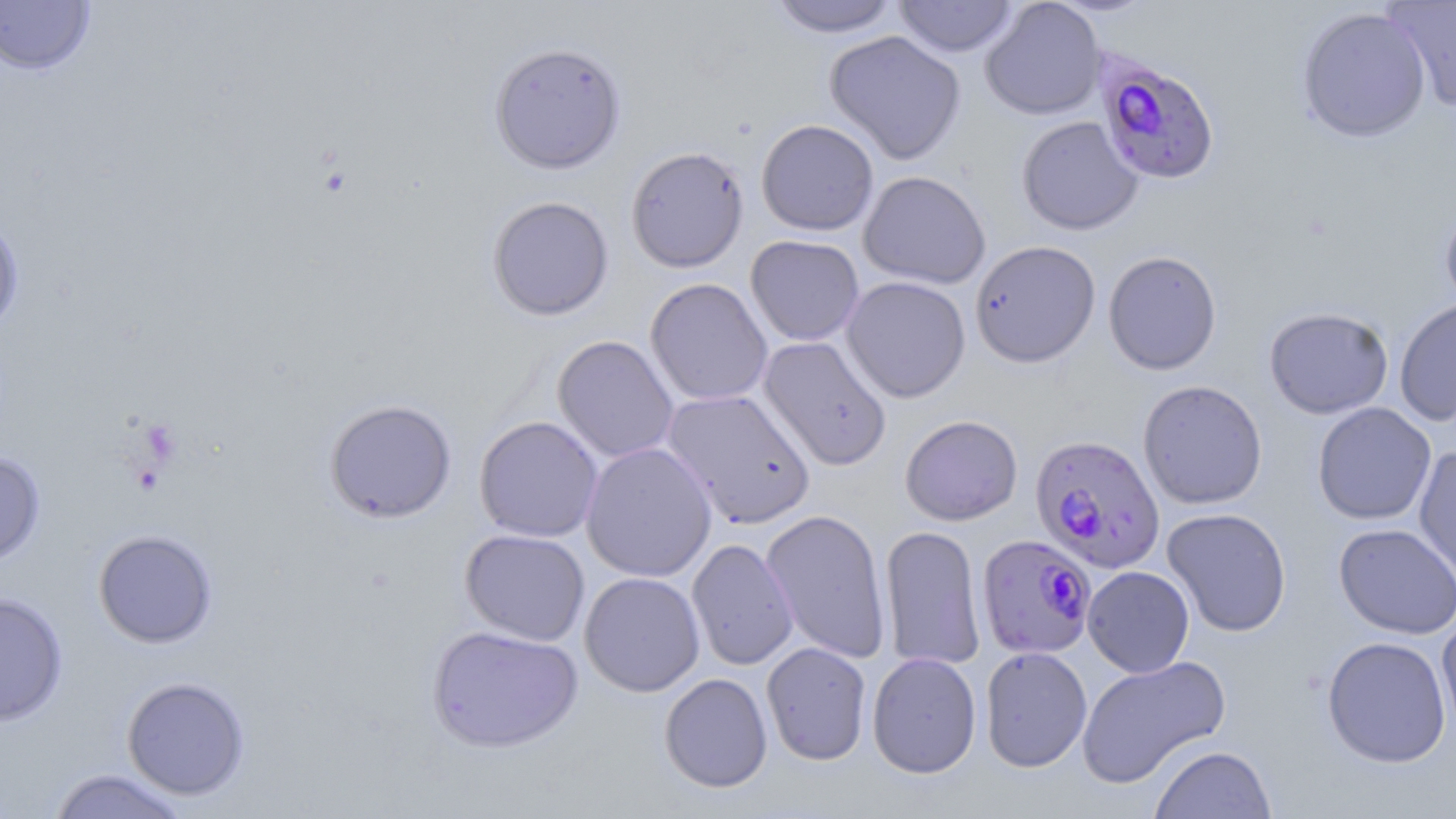 Approximate bounding boxes as (x1,y1)-(x2,y2) corner pairs in pixels. Uninfected red blood cell locations: (766,0)-(902,37), (893,0)-(1020,58), (980,0)-(1106,120), (1383,0)-(1456,109), (0,1)-(96,77), (1296,6)-(1432,144), (824,30)-(966,165), (488,41)-(627,174), (1016,115)-(1143,235), (756,118)-(878,236), (625,145)-(749,273), (858,171)-(991,289), (486,195)-(615,321), (1439,202)-(1456,315), (0,214)-(25,337), (745,235)-(865,346), (969,240)-(1101,368), (1103,250)-(1222,375), (841,276)-(971,403), (645,277)-(773,406), (1394,298)-(1456,426), (1264,307)-(1394,419), (552,335)-(679,463), (757,336)-(892,471), (1138,379)-(1268,509), (662,389)-(816,529), (324,398)-(457,524), (1312,402)-(1436,525), (900,414)-(1023,526), (474,416)-(604,542), (580,442)-(717,582), (1413,445)-(1456,589), (0,452)-(46,566), (1162,507)-(1292,637), (760,509)-(892,663), (1334,523)-(1456,639), (879,524)-(986,670), (460,528)-(590,646), (93,529)-(218,648), (686,538)-(799,671), (1082,566)-(1195,677), (579,571)-(706,697), (0,591)-(69,726), (1436,614)-(1456,740), (426,625)-(583,753), (1322,635)-(1452,767), (761,642)-(872,765), (979,646)-(1092,772), (866,652)-(982,778), (1076,655)-(1231,788), (659,672)-(773,793), (121,675)-(251,800), (1149,744)-(1276,818), (46,768)-(191,818). Plasmodium falciparum-infected red blood cell locations: (1093,51)-(1221,186), (1030,434)-(1165,573), (976,533)-(1097,659). Slide-level diagnosis: Plasmodium falciparum. Thin blood smear. Light microscopy. Single field of view. Image is 1456×819 pixels. Captured at 1000x magnification. May-Grünwald-Giemsa-stained preparation.